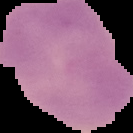
Result: no Plasmodium parasites seen. The area outside the segmented cell region is set to black. Image is 133×133 pixels. From a thin blood film.